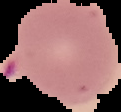

From a thin blood film. Image is 121×112 pixels. Cell region segmented out of the field of view; the surrounding area is masked to black. Result: no Plasmodium parasites detected.